Comment on the morphology of the erythrocytes.
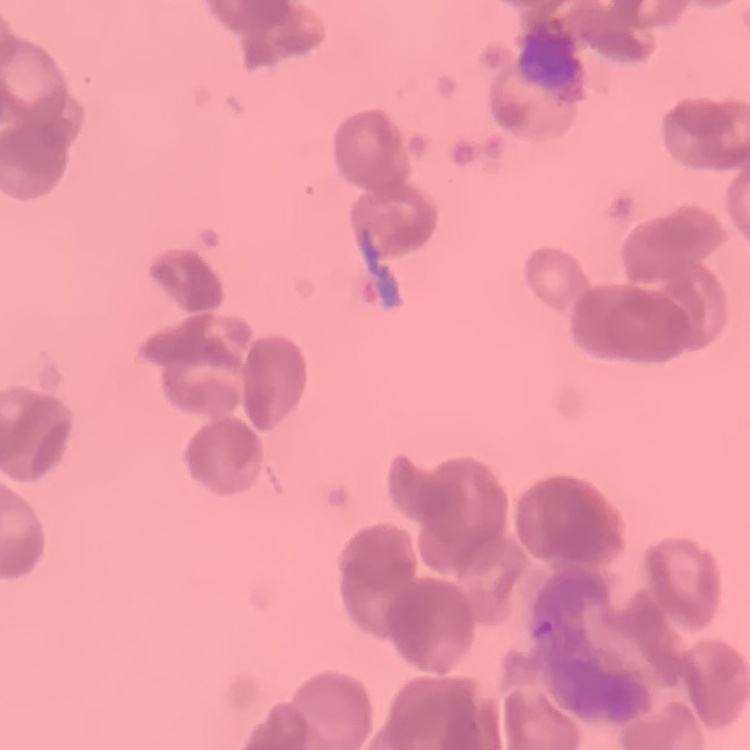
Rouleaux formation.

Summary:
  - Image type: square crop of a larger photomicrograph
  - Stain: Field's or Giemsa
  - Preparation: thin blood film